Assess this cell for malaria.
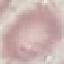

Uninfected.

image type = automatically extracted cell patch, resized to 64 × 64 pixels
stain = Giemsa
capture = smartphone camera at the microscope eyepiece
preparation = thin blood smear